Classify this cell by malaria status.
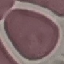
It is uninfected.

capture = smartphone camera at the microscope eyepiece
preparation = thin blood film
image type = cell patch, automatically extracted from a larger field of view and resized to 64 × 64 pixels
stain = Giemsa